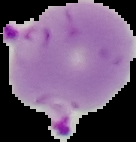
The area outside the segmented cell region is set to black. From a thin blood film. Result: malaria parasites identified. Image is 136×142 pixels.